Name the cell type shown.
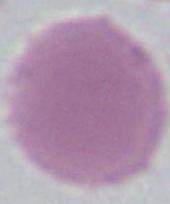

An erythrocyte.

modality = micrograph
magnification = 1000x